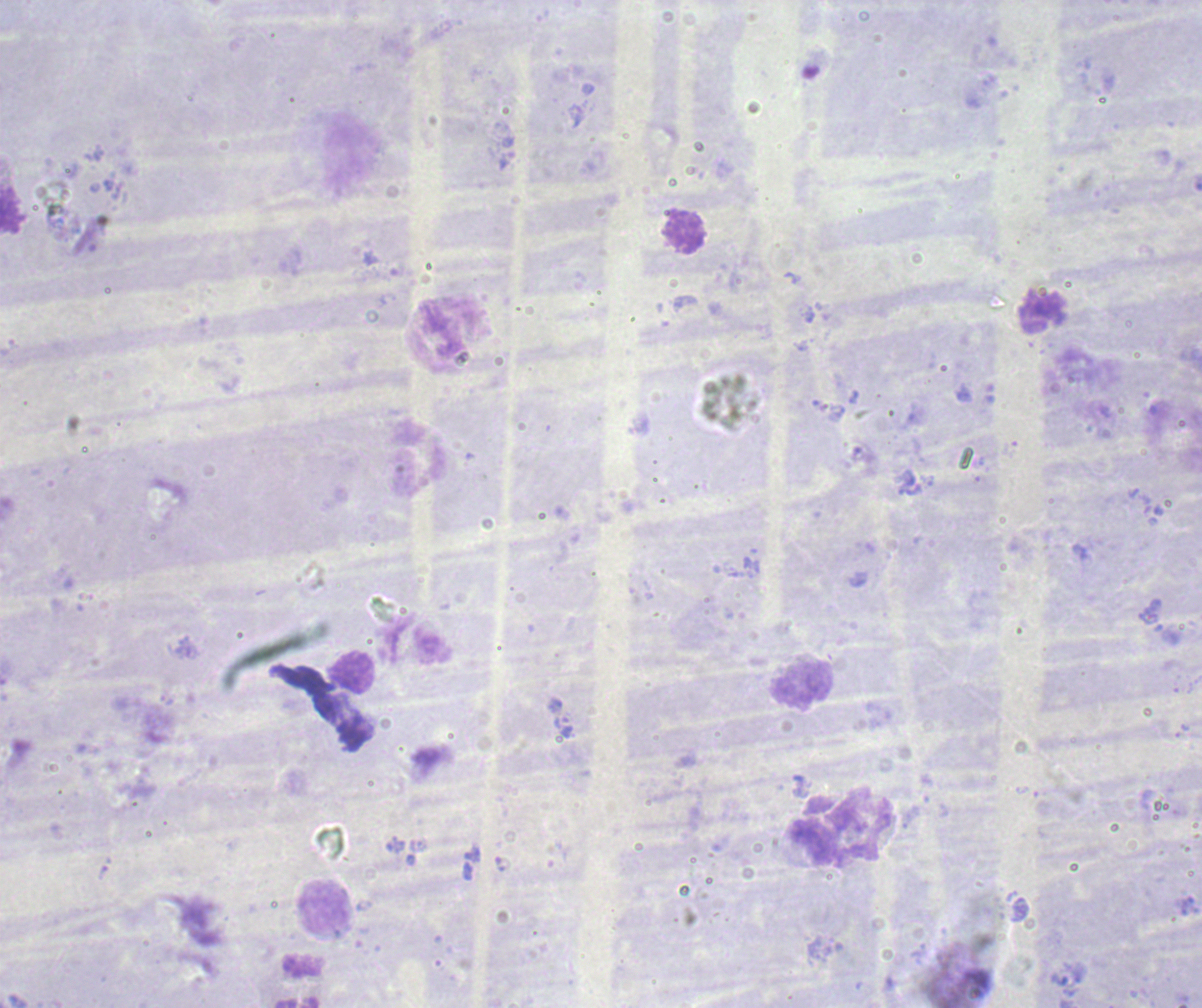

Approximate centers as {x, y} in pixels.
Summary:
  - Trophozoite locations: {563, 726}
  - Leukocyte locations: {350, 151}, {422, 459}, {354, 673}, {802, 685}, {860, 829}, {325, 908}
  - Result: Plasmodium parasites detected
  - Preparation: thick blood smear
  - Magnification: 100x
  - Stain: Romanowsky
  - Context: previously used in a real diagnosis
  - Field of view: single
  - Background quality: poor
  - Image size: 1202×1008 pixels